Outline each uninfected red blood cell.
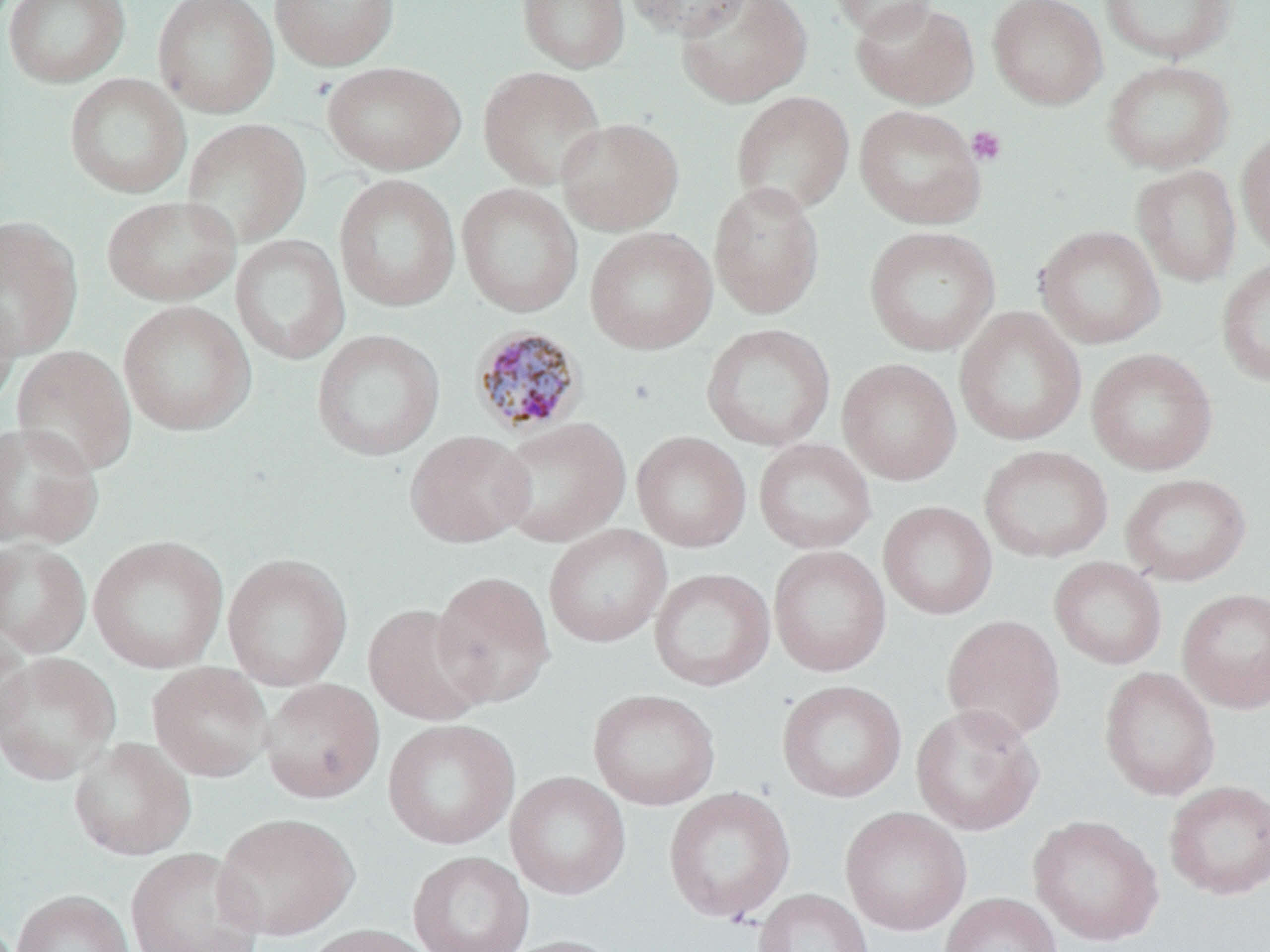

Approximate bounding boxes as [x1, y1, x2, y2] in pixels.
Uninfected red blood cells: [2, 0, 131, 88], [152, 0, 279, 118], [269, 0, 400, 71], [516, 0, 631, 73], [622, 0, 753, 40], [675, 0, 813, 108], [827, 0, 941, 39], [987, 0, 1108, 109], [1098, 0, 1238, 63], [851, 1, 980, 109], [1101, 59, 1235, 175], [321, 61, 466, 175], [478, 65, 607, 190], [64, 73, 191, 198], [731, 91, 855, 216], [855, 104, 986, 229], [555, 116, 684, 236], [181, 117, 312, 247], [1236, 126, 1270, 261], [1131, 164, 1242, 286], [334, 173, 461, 313], [708, 180, 825, 320], [456, 183, 583, 317], [101, 195, 240, 306], [0, 216, 83, 359], [863, 225, 1000, 356], [1034, 225, 1166, 350], [585, 226, 717, 354], [230, 234, 350, 365], [1216, 257, 1270, 386], [0, 285, 21, 415], [118, 300, 256, 437], [953, 306, 1087, 447], [701, 323, 836, 451], [310, 328, 445, 461], [11, 345, 137, 478], [1086, 348, 1218, 476], [837, 358, 962, 486], [494, 417, 631, 547], [0, 422, 103, 550], [405, 430, 535, 548], [631, 431, 751, 552], [753, 438, 877, 554], [979, 445, 1113, 563], [1120, 472, 1252, 586], [877, 501, 997, 619], [543, 524, 672, 648], [87, 534, 229, 674], [0, 538, 92, 658], [768, 545, 891, 677], [222, 553, 353, 691], [1049, 557, 1168, 670], [648, 567, 776, 692], [431, 570, 556, 709], [1176, 587, 1270, 713], [363, 602, 491, 727], [941, 614, 1066, 744], [0, 621, 33, 750], [0, 651, 122, 786], [147, 662, 274, 781], [1099, 667, 1221, 801], [260, 678, 385, 803], [776, 679, 907, 803], [588, 689, 721, 811], [910, 703, 1045, 835], [382, 718, 520, 850], [68, 737, 196, 861], [505, 771, 631, 900], [1163, 779, 1270, 900], [663, 786, 795, 923], [840, 806, 972, 936], [213, 812, 358, 940], [1028, 814, 1164, 946], [126, 848, 264, 952], [408, 850, 534, 952], [753, 888, 874, 952], [11, 889, 134, 952], [939, 892, 1062, 952], [301, 922, 439, 952], [496, 934, 627, 952].

slide-level diagnosis = Plasmodium malariae
stain = May-Grünwald-Giemsa
preparation = thin blood smear
field of view = one of a larger specimen
modality = optical microscopy
Plasmodium malariae-infected red blood cell locations = approximate bounding boxes as [x1, y1, x2, y2] in pixels: [469, 324, 587, 436]
platelet locations = approximate bounding boxes as [x1, y1, x2, y2] in pixels: [966, 125, 1007, 166]
magnification = 1000x
image size = 1270×952 pixels